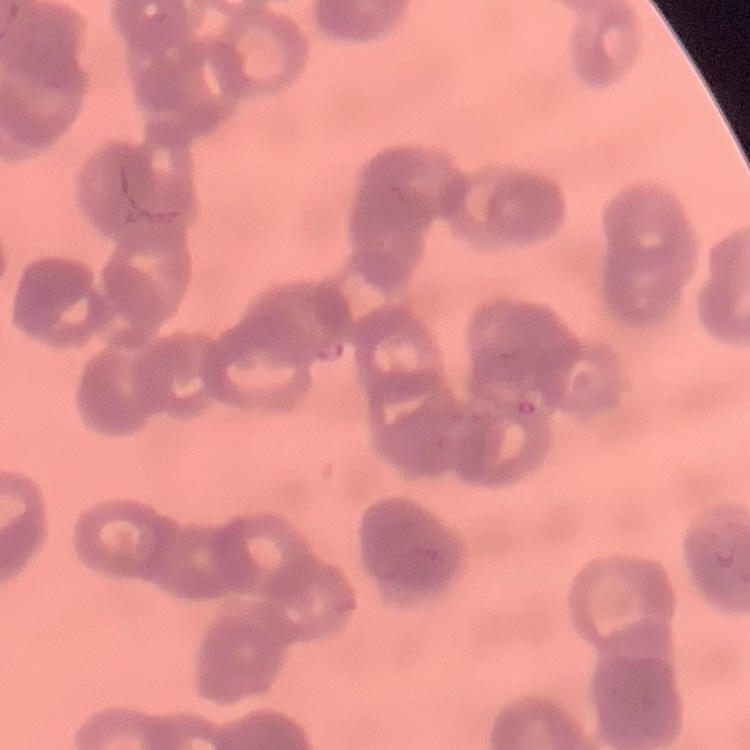
erythrocyte morphology = rouleaux formation
stain = Field's or Giemsa
image type = square crop of a larger photomicrograph
preparation = thin blood film